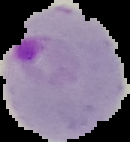
Summary:
  - Preparation: thin blood film
  - Image size: 130×142 pixels
  - Malaria status: parasitized
  - Image type: segmented cell region with the area outside set to black